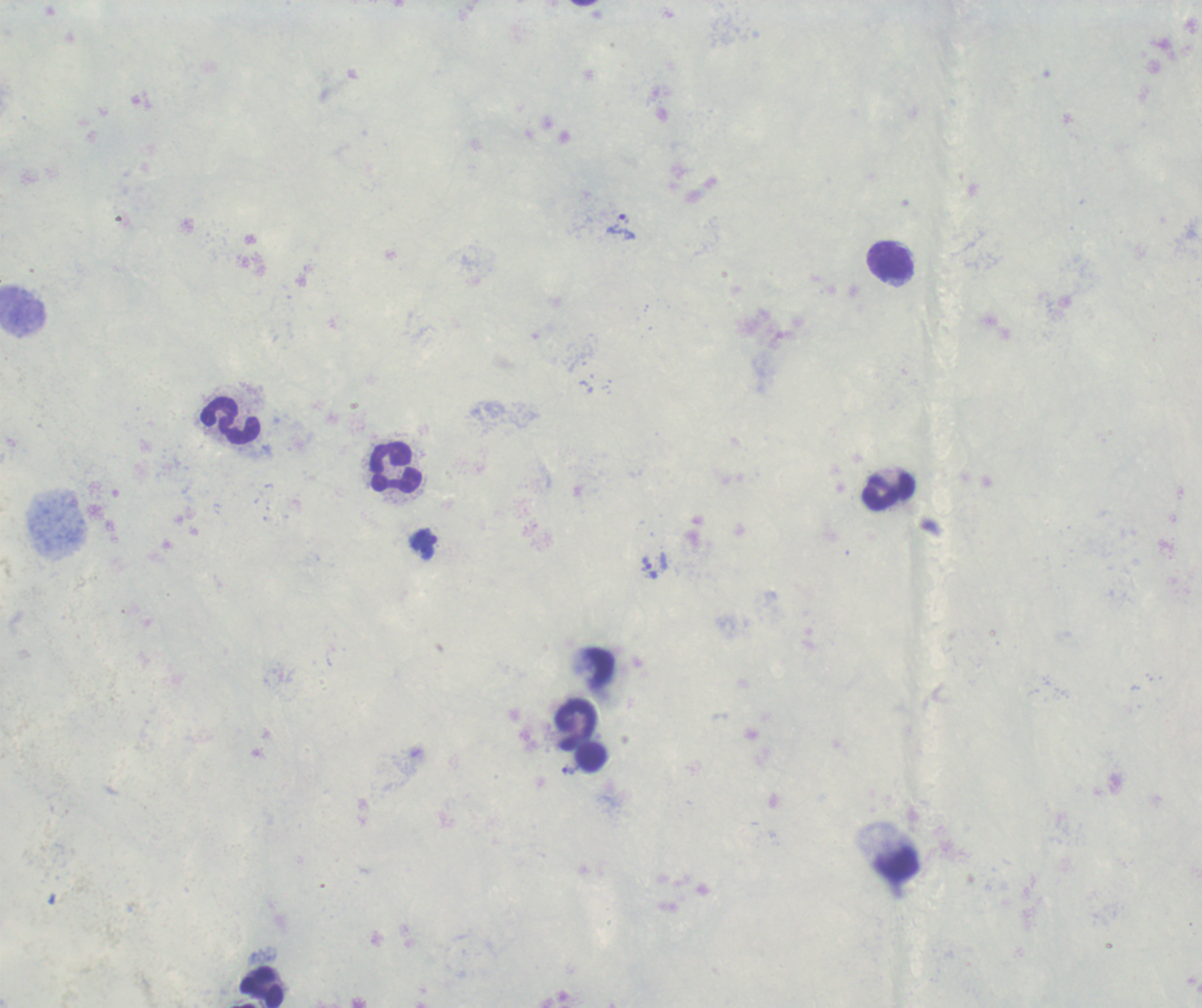 Approximate object centers, in pixels from the top-left corner. Trophozoite locations: (x=622, y=227), (x=646, y=563), (x=568, y=769). Leukocyte locations: (x=891, y=261), (x=22, y=308), (x=230, y=421), (x=397, y=467), (x=887, y=492), (x=575, y=722), (x=591, y=757), (x=263, y=988). Coloration quality: good. 100x magnification. Romanowsky-stained preparation. Image is 1202×1008 pixels. Background quality: poor. Result: malaria parasites identified. Single field of view. Previously used in a real diagnosis. Thick blood film.